Report the malaria status of this cell.
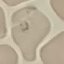
Parasitized.

Cell patch, automatically extracted from a larger field of view and resized to 64 × 64 pixels. Giemsa stain. Thin smear of blood. Photographed with a smartphone camera at the microscope eyepiece.